Assess this cell for malaria.
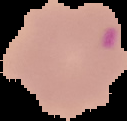

It is uninfected.

{
  "image_type": "segmented cell region with the area outside set to black",
  "image_size": "127×121 pixels",
  "preparation": "thin blood film"
}